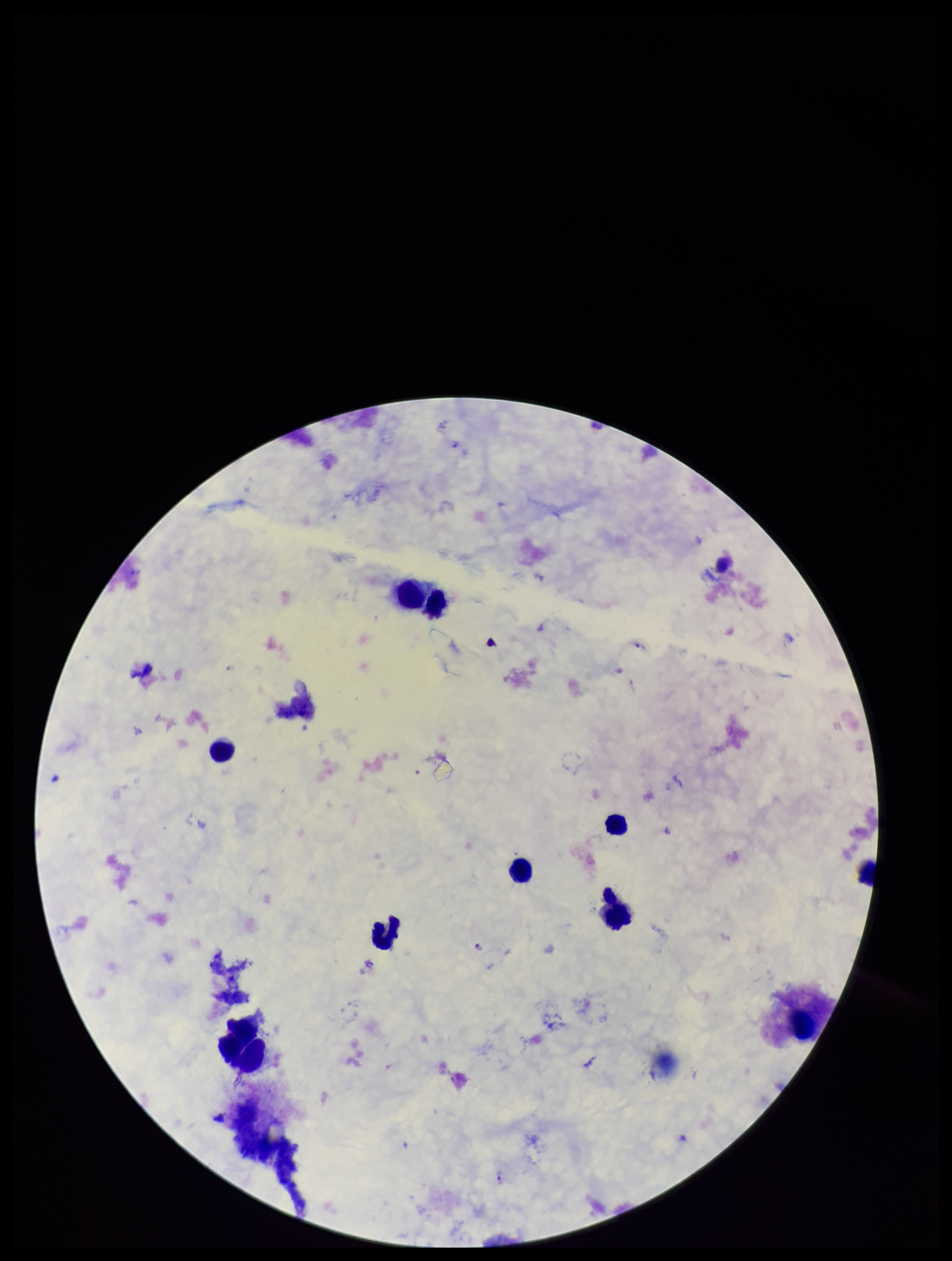
Parasite count: 7. One field from this slide. Smartphone photograph taken through the eyepiece of a microscope. Species reported for this patient: Plasmodium falciparum. Preparation: thick blood smear. Giemsa stain. Patient malaria status: positive. Image is 952×1261 pixels. Plasmodium parasites: identified. Leukocyte count: 8.